Assess this cell for malaria.
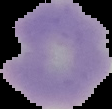

Uninfected.

image_type: segmented cell region with the area outside set to black
image_size: 112×109 pixels
preparation: thin blood smear